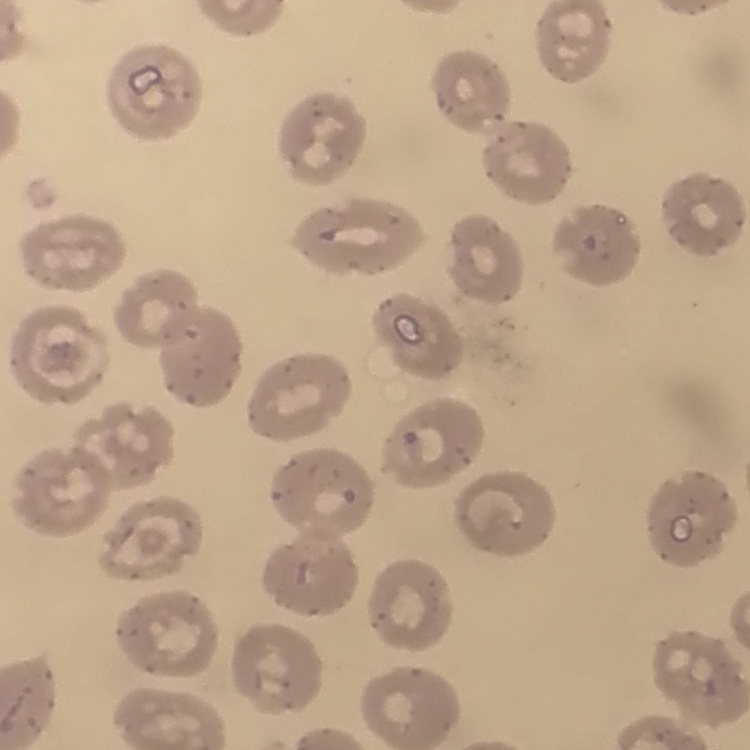

red blood cell morphology = no rouleaux formation
preparation = thin blood smear
image type = one tile cut from a larger photomicrograph
stain = Field's or Giemsa